Comment on the morphology of the erythrocytes.
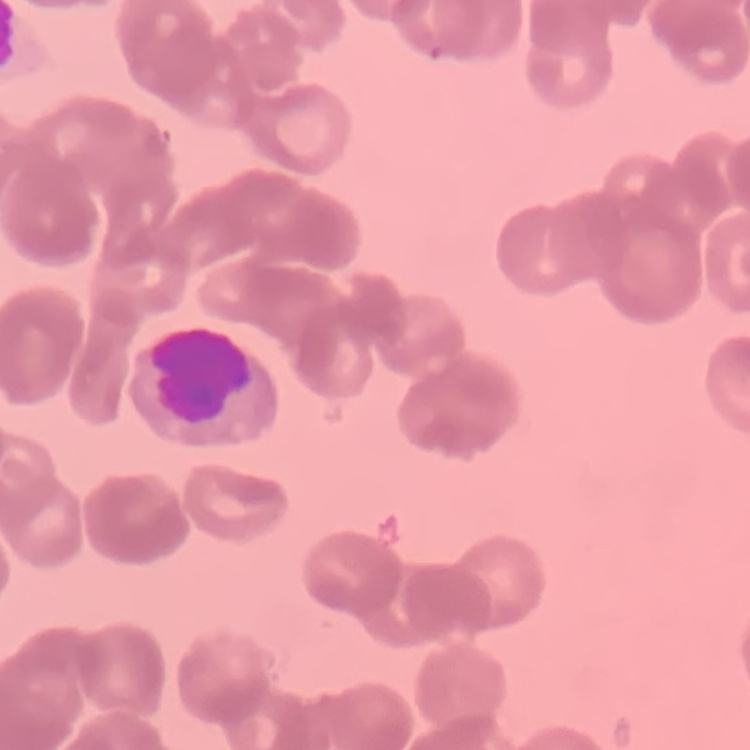
They show rouleaux formation.

Thin blood smear. One tile cut from a larger photomicrograph. Stained with either Field's or Giemsa.